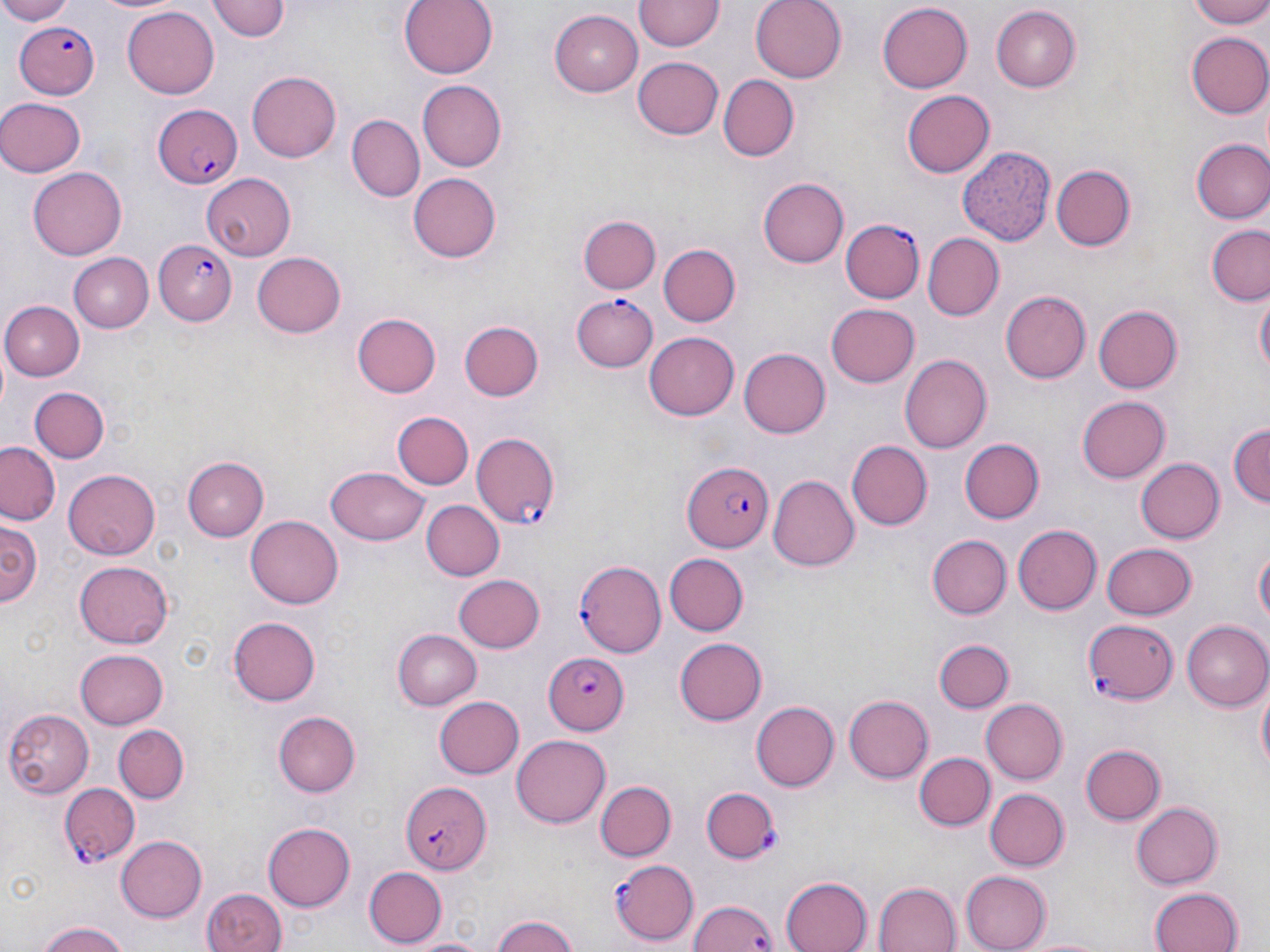
slide-level diagnosis = Plasmodium falciparum
field of view = single
uninfected red blood cell locations = approximate bounding boxes as (x1,y1)-(x2,y2) corner pairs in pixels: (0,0)-(75,24), (91,0)-(182,15), (212,0)-(290,41), (400,0)-(498,79), (637,0)-(722,52), (751,0)-(847,83), (1186,0)-(1270,27), (878,1)-(972,90), (122,4)-(219,97), (992,6)-(1082,92), (550,9)-(643,94), (1184,31)-(1270,119), (633,58)-(722,141), (248,69)-(341,161), (719,75)-(798,160), (417,81)-(508,171), (901,90)-(993,177), (0,97)-(84,177), (347,115)-(423,200), (1191,139)-(1270,223), (960,147)-(1058,247), (1051,165)-(1133,251), (29,166)-(128,259), (200,172)-(295,261), (408,172)-(502,263), (757,177)-(847,268), (580,216)-(660,294), (1205,225)-(1270,306), (921,234)-(1002,321), (656,240)-(741,326), (251,251)-(345,338), (70,253)-(152,332), (1000,290)-(1091,384), (1255,290)-(1269,378), (4,300)-(83,380), (826,304)-(921,388), (1092,305)-(1182,394), (353,311)-(440,397), (458,320)-(544,403), (644,331)-(740,419), (738,348)-(830,439), (900,354)-(992,455), (29,387)-(110,463), (1076,396)-(1170,483), (393,412)-(474,489), (1228,418)-(1270,509), (960,439)-(1044,522), (849,440)-(934,530), (0,441)-(62,524), (1135,456)-(1225,544), (183,457)-(268,541), (65,466)-(163,557), (324,466)-(431,545), (770,473)-(860,572), (422,500)-(504,581), (246,515)-(341,609), (1,522)-(40,614), (1011,524)-(1100,615), (929,534)-(1010,618), (1100,542)-(1197,619), (1255,545)-(1269,631), (663,552)-(748,635), (72,561)-(175,651), (453,574)-(545,653), (227,615)-(321,708), (1182,620)-(1270,711), (393,629)-(483,710), (675,635)-(767,723), (933,636)-(1014,715), (75,647)-(169,727), (1256,681)-(1269,778), (845,694)-(937,783), (433,695)-(524,780), (979,698)-(1067,785), (751,700)-(839,791), (2,707)-(93,796), (272,709)-(359,798), (113,724)-(189,802), (511,734)-(612,829), (1081,743)-(1164,825), (914,751)-(994,833), (594,780)-(676,861), (985,789)-(1069,872), (1131,800)-(1221,890), (263,821)-(355,912), (116,835)-(207,921), (363,866)-(445,947), (961,870)-(1052,951), (780,874)-(871,952), (874,880)-(963,952), (200,888)-(288,952), (1150,888)-(1242,952), (489,913)-(581,952), (35,920)-(131,952), (1024,933)-(1107,952)
Plasmodium falciparum-infected red blood cell locations = approximate bounding boxes as (x1,y1)-(x2,y2) corner pairs in pixels: (13,20)-(100,99), (151,101)-(245,189), (840,219)-(924,303), (154,238)-(236,325), (570,295)-(657,373), (472,431)-(561,527), (681,460)-(772,554), (573,545)-(668,655), (1083,621)-(1180,706), (542,653)-(628,733), (401,780)-(491,873), (58,783)-(141,864), (700,788)-(779,864), (611,859)-(699,945), (689,896)-(778,951)
preparation = thin blood film
magnification = 1000x
stain = May-Grünwald-Giemsa
modality = light microscopy
image size = 1270×952 pixels